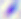 Photomicrograph. Captured at 400x magnification. Toxoplasma gondii is seen.